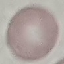

{
  "malaria_status": "uninfected",
  "stain": "Giemsa",
  "capture": "smartphone through the microscope eyepiece",
  "preparation": "thin blood film",
  "image_type": "cell patch, automatically extracted from a larger field of view and resized to 64 × 64 pixels"
}